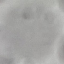

result = no malaria parasites seen
preparation = thin blood film
image type = automatically extracted cell patch, resized to 64 × 64 pixels
capture = smartphone camera at the microscope eyepiece
stain = Giemsa